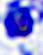

Summary:
  - Modality: photomicrograph
  - Identification: leukocyte
  - Magnification: 400x